Name the parasite shown.
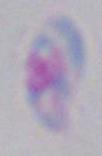

Toxoplasma gondii.

Summary:
  - Magnification: 1000x
  - Modality: micrograph